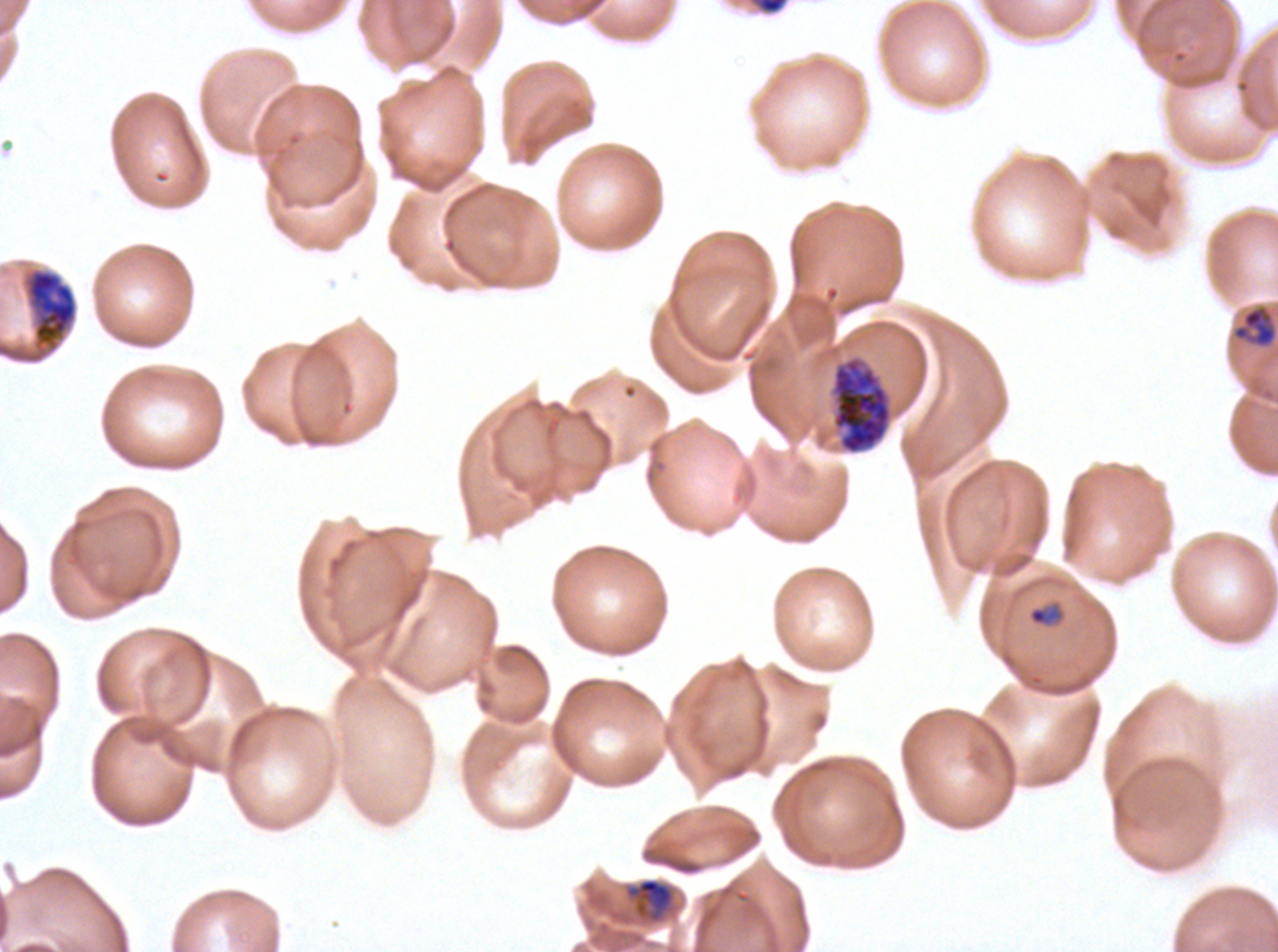

field_of_view: sub-image separated from a larger composite
early_schizont_locations: 'approximate bounding boxes as {x1, y1, x2, y2} in pixels: {24, 268, 78, 352}, {829, 355, 892, 455}'
stain: Giemsa
image_size: 1278×952 pixels
life_cycle_stages_observed: late-ring/early-trophozoite, mid trophozoite, early schizont
debris_locations: 'approximate bounding boxes as {x1, y1, x2, y2} in pixels: {748, 0, 789, 15}'
preparation: thin blood film
mid_trophozoite_locations: 'approximate bounding boxes as {x1, y1, x2, y2} in pixels: {626, 877, 674, 921}'
late_ring_early_trophozoite_locations: 'approximate bounding boxes as {x1, y1, x2, y2} in pixels: {1232, 305, 1277, 348}, {1027, 605, 1063, 627}'
specimen: Plasmodium falciparum cultured ex vivo for 24 to 48 hours, from a patient in The Gambia